Identify the parasite.
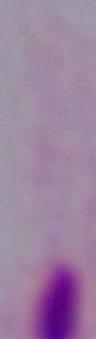
A trichomonad.

{
  "modality": "micrograph",
  "magnification": "1000x"
}